Assess this cell for malaria.
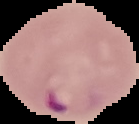
Parasitized.

{
  "image_size": "139×124 pixels",
  "preparation": "thin blood smear",
  "image_type": "cell region segmented out of the field of view; surrounding area masked to black"
}